Name the parasite shown.
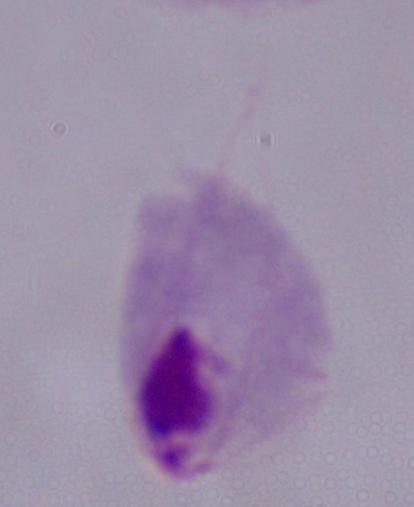
A trichomonad.

Photomicrograph. Captured at 1000x magnification.